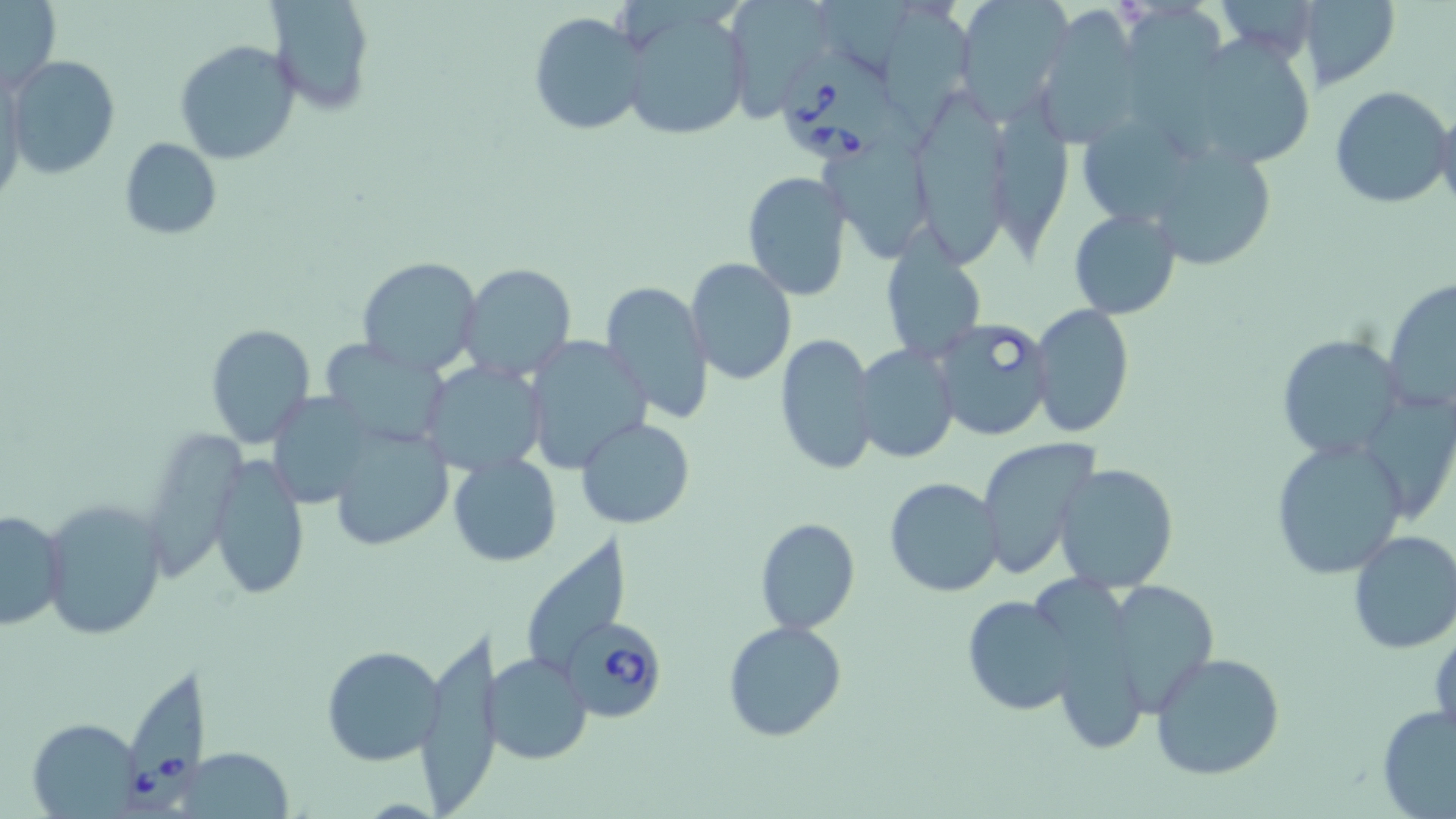
Summary:
  - Coordinate format: approximate bounding boxes as named x1/y1/x2/y2 corners in pixels
  - Babesia divergens-infected red blood cell locations: (x1=776, y1=50, x2=903, y2=164), (x1=932, y1=316, x2=1055, y2=443), (x1=564, y1=619, x2=669, y2=722), (x1=124, y1=664, x2=207, y2=814)
  - Uninfected red blood cell locations: (x1=0, y1=0, x2=62, y2=94), (x1=267, y1=0, x2=377, y2=114), (x1=724, y1=0, x2=835, y2=121), (x1=876, y1=0, x2=973, y2=132), (x1=951, y1=0, x2=1071, y2=120), (x1=1299, y1=2, x2=1398, y2=92), (x1=615, y1=4, x2=751, y2=143), (x1=1127, y1=4, x2=1236, y2=160), (x1=1032, y1=6, x2=1145, y2=146), (x1=527, y1=10, x2=649, y2=137), (x1=1202, y1=34, x2=1310, y2=167), (x1=175, y1=40, x2=300, y2=165), (x1=6, y1=56, x2=120, y2=180), (x1=1330, y1=85, x2=1452, y2=208), (x1=994, y1=87, x2=1079, y2=256), (x1=923, y1=102, x2=1021, y2=267), (x1=1434, y1=108, x2=1456, y2=219), (x1=1087, y1=118, x2=1194, y2=220), (x1=119, y1=137, x2=222, y2=241), (x1=823, y1=138, x2=935, y2=263), (x1=1163, y1=151, x2=1272, y2=270), (x1=741, y1=172, x2=853, y2=301), (x1=1068, y1=208, x2=1181, y2=319), (x1=880, y1=236, x2=986, y2=365), (x1=356, y1=255, x2=481, y2=375), (x1=685, y1=257, x2=797, y2=386), (x1=459, y1=263, x2=578, y2=383), (x1=1382, y1=276, x2=1456, y2=416), (x1=599, y1=280, x2=714, y2=423), (x1=1030, y1=303, x2=1134, y2=439), (x1=204, y1=323, x2=315, y2=446), (x1=774, y1=331, x2=879, y2=476), (x1=523, y1=334, x2=654, y2=472), (x1=1275, y1=334, x2=1404, y2=460), (x1=323, y1=342, x2=446, y2=441), (x1=853, y1=344, x2=960, y2=462), (x1=421, y1=360, x2=548, y2=477), (x1=267, y1=386, x2=370, y2=503), (x1=1366, y1=386, x2=1456, y2=519), (x1=579, y1=418, x2=694, y2=529), (x1=149, y1=424, x2=237, y2=576), (x1=326, y1=425, x2=454, y2=551), (x1=976, y1=437, x2=1105, y2=583), (x1=1269, y1=437, x2=1409, y2=580), (x1=449, y1=453, x2=562, y2=567), (x1=209, y1=455, x2=310, y2=600), (x1=1055, y1=463, x2=1178, y2=593), (x1=883, y1=477, x2=1004, y2=598), (x1=38, y1=497, x2=167, y2=641), (x1=1, y1=507, x2=68, y2=632), (x1=755, y1=518, x2=859, y2=635), (x1=1346, y1=529, x2=1456, y2=654), (x1=1100, y1=578, x2=1219, y2=719), (x1=962, y1=595, x2=1082, y2=716), (x1=723, y1=620, x2=848, y2=743), (x1=415, y1=624, x2=497, y2=809), (x1=322, y1=644, x2=448, y2=767), (x1=485, y1=652, x2=593, y2=764), (x1=1152, y1=652, x2=1286, y2=780), (x1=1377, y1=703, x2=1456, y2=818), (x1=26, y1=719, x2=142, y2=815)
  - Slide-level diagnosis: Babesia divergens
  - Magnification: 1000x
  - Image size: 1456×819 pixels
  - Modality: light microscopy
  - Stain: May-Grünwald-Giemsa
  - Field of view: single
  - Preparation: thin blood smear